Name the parasite shown.
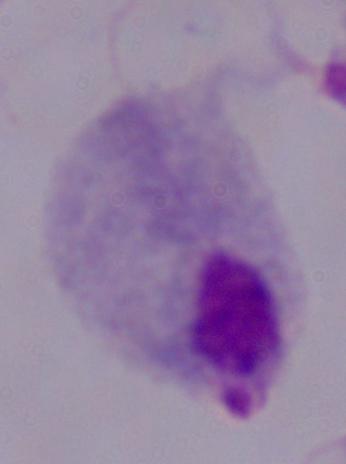

This is a trichomonad.

magnification = 1000x
modality = photomicrograph